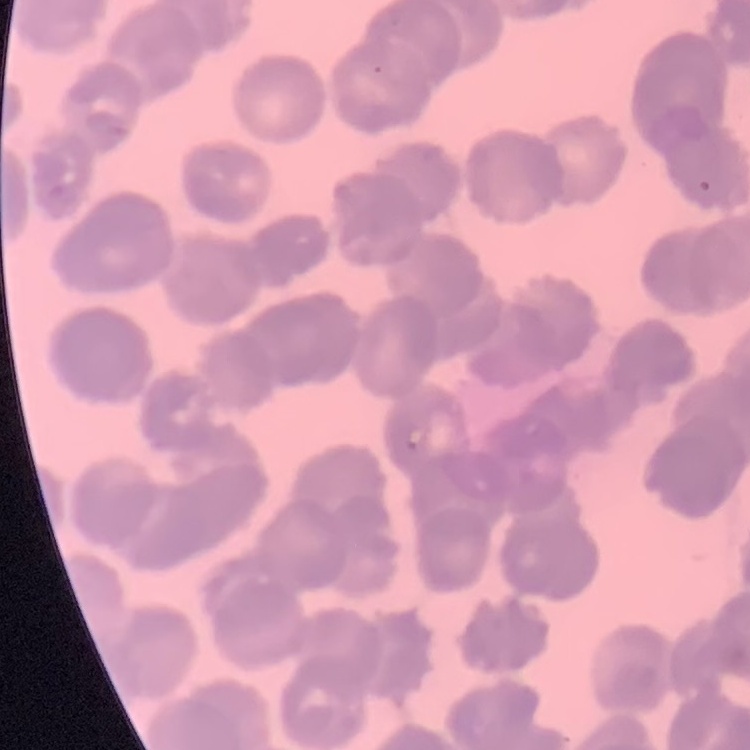
erythrocyte_morphology: rouleaux formation
preparation: thin blood film
image_type: square crop of a larger photomicrograph
stain: Field's or Giemsa